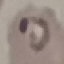
Result: malaria parasites identified. Thin blood smear. Acquired by smartphone through the microscope eyepiece. Automatically extracted cell patch, resized to 64 × 64 pixels. Giemsa-stained preparation.